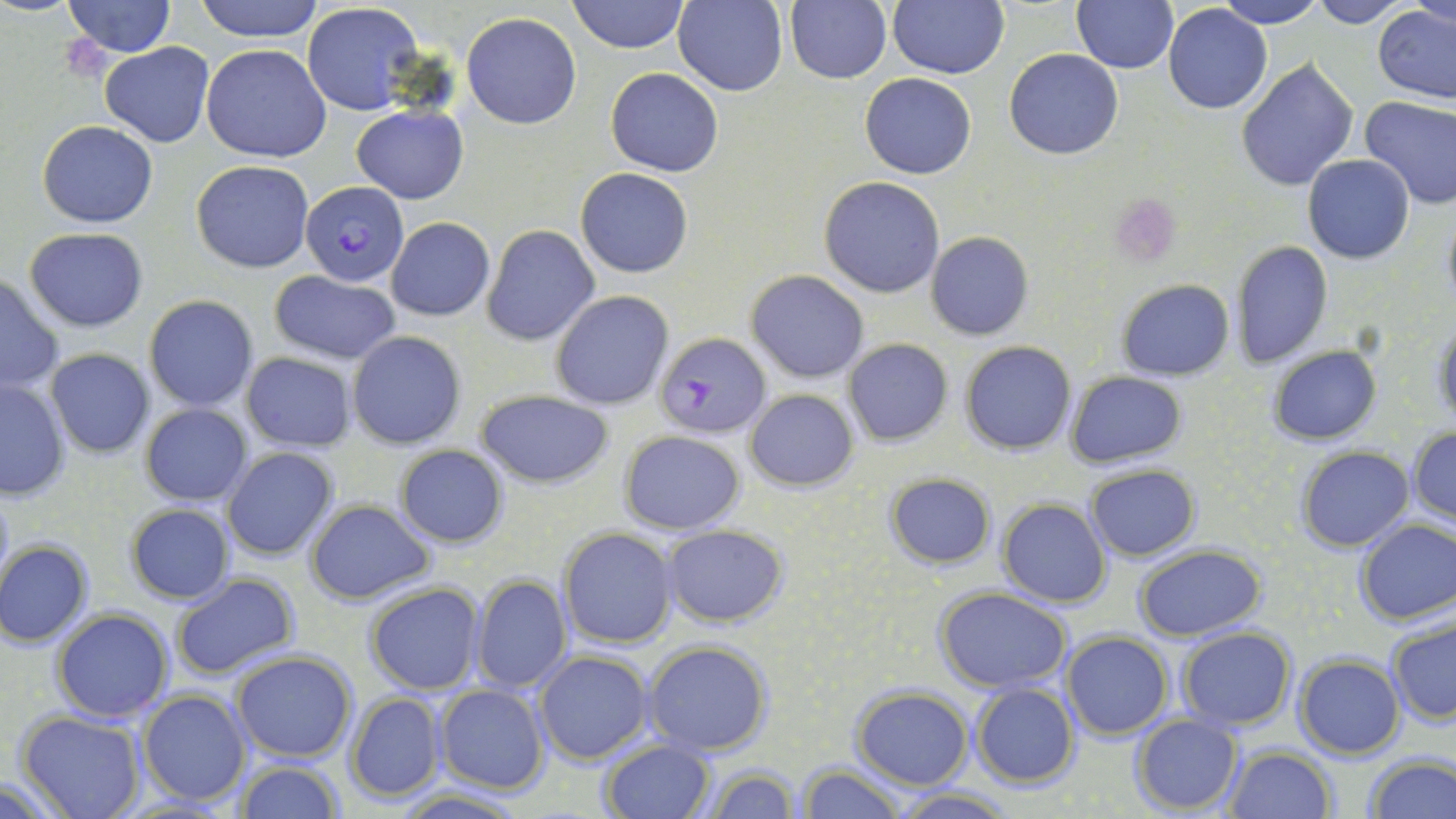

Summary:
  - Coordinate format: approximate bounding boxes as [x1, y1, x2, y2] in pixels
  - Uninfected red blood cell locations: [62, 0, 175, 57], [194, 0, 326, 42], [568, 0, 688, 54], [673, 0, 788, 96], [786, 0, 892, 85], [888, 0, 1008, 78], [1211, 0, 1328, 27], [1305, 0, 1411, 27], [1410, 0, 1456, 31], [1071, 1, 1178, 73], [302, 2, 423, 115], [1163, 4, 1274, 115], [1373, 5, 1455, 104], [462, 11, 582, 129], [98, 43, 215, 146], [200, 44, 332, 163], [1004, 49, 1124, 159], [1237, 59, 1359, 193], [606, 68, 724, 177], [859, 72, 977, 179], [1358, 95, 1456, 211], [351, 105, 470, 203], [38, 121, 157, 229], [1302, 154, 1414, 264], [190, 160, 314, 272], [575, 168, 692, 277], [820, 176, 944, 297], [1441, 207, 1456, 311], [386, 217, 495, 321], [483, 225, 600, 345], [23, 227, 149, 331], [926, 231, 1034, 340], [1232, 240, 1333, 368], [257, 270, 386, 446], [747, 270, 868, 383], [268, 271, 402, 364], [1, 273, 65, 393], [1116, 279, 1234, 380], [550, 291, 672, 410], [143, 294, 259, 412], [1433, 317, 1456, 430], [346, 331, 467, 448], [843, 338, 953, 446], [961, 341, 1075, 454], [1268, 346, 1381, 444], [44, 348, 155, 459], [240, 351, 358, 451], [1064, 371, 1187, 469], [0, 377, 71, 500], [475, 389, 615, 489], [747, 389, 858, 491], [140, 403, 252, 507], [1407, 427, 1456, 525], [619, 429, 745, 533], [393, 444, 509, 548], [222, 447, 340, 561], [1296, 447, 1414, 550], [1084, 464, 1202, 561], [885, 474, 996, 567], [0, 477, 14, 596], [305, 499, 435, 603], [997, 499, 1110, 606], [125, 502, 234, 603], [1355, 518, 1455, 625], [661, 525, 787, 627], [558, 528, 678, 649], [1, 540, 92, 648], [1134, 544, 1266, 639], [169, 573, 301, 680], [471, 574, 572, 693], [364, 583, 485, 697], [934, 588, 1072, 692], [51, 606, 174, 723], [1387, 616, 1455, 726], [1176, 627, 1295, 731], [1062, 632, 1172, 740], [643, 641, 773, 755], [230, 649, 359, 764], [533, 649, 654, 764], [1293, 654, 1405, 759], [970, 683, 1079, 787], [435, 684, 549, 793], [852, 686, 973, 790], [137, 688, 252, 806], [344, 692, 448, 804], [16, 712, 146, 819], [1128, 714, 1243, 816], [599, 739, 714, 819], [1224, 744, 1336, 819], [1364, 754, 1456, 819], [236, 759, 344, 818], [699, 763, 798, 819], [797, 764, 905, 819], [0, 776, 76, 819], [392, 787, 533, 819], [894, 788, 1013, 817]
  - Platelet locations: [1110, 193, 1183, 268]
  - Plasmodium falciparum-infected red blood cell locations: [300, 181, 410, 285], [654, 331, 771, 440]
  - Slide-level diagnosis: Plasmodium falciparum
  - Modality: light microscopy
  - Field of view: single
  - Stain: May-Grünwald-Giemsa
  - Magnification: 1000x
  - Image size: 1456×819 pixels
  - Preparation: thin blood film